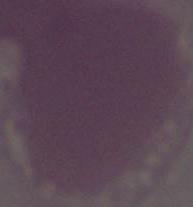

1000x magnification. Micrograph. A red blood cell is shown.